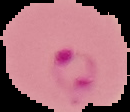

The area outside the segmented cell region is set to black. Malaria status: parasitized. Image is 130×112 pixels. From a thin blood smear.